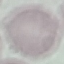
Result: no malaria parasites detected. Acquired by smartphone through the microscope eyepiece. Cell patch, automatically extracted from a larger field of view and resized to 64 × 64 pixels. Thin blood smear. Giemsa-stained preparation.